Report the malaria status of this cell.
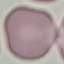

Uninfected.

capture: smartphone through the microscope eyepiece
stain: Giemsa
image_type: automatically extracted cell patch, resized to 64 × 64 pixels
preparation: thin blood film